Point out each leukocyte.
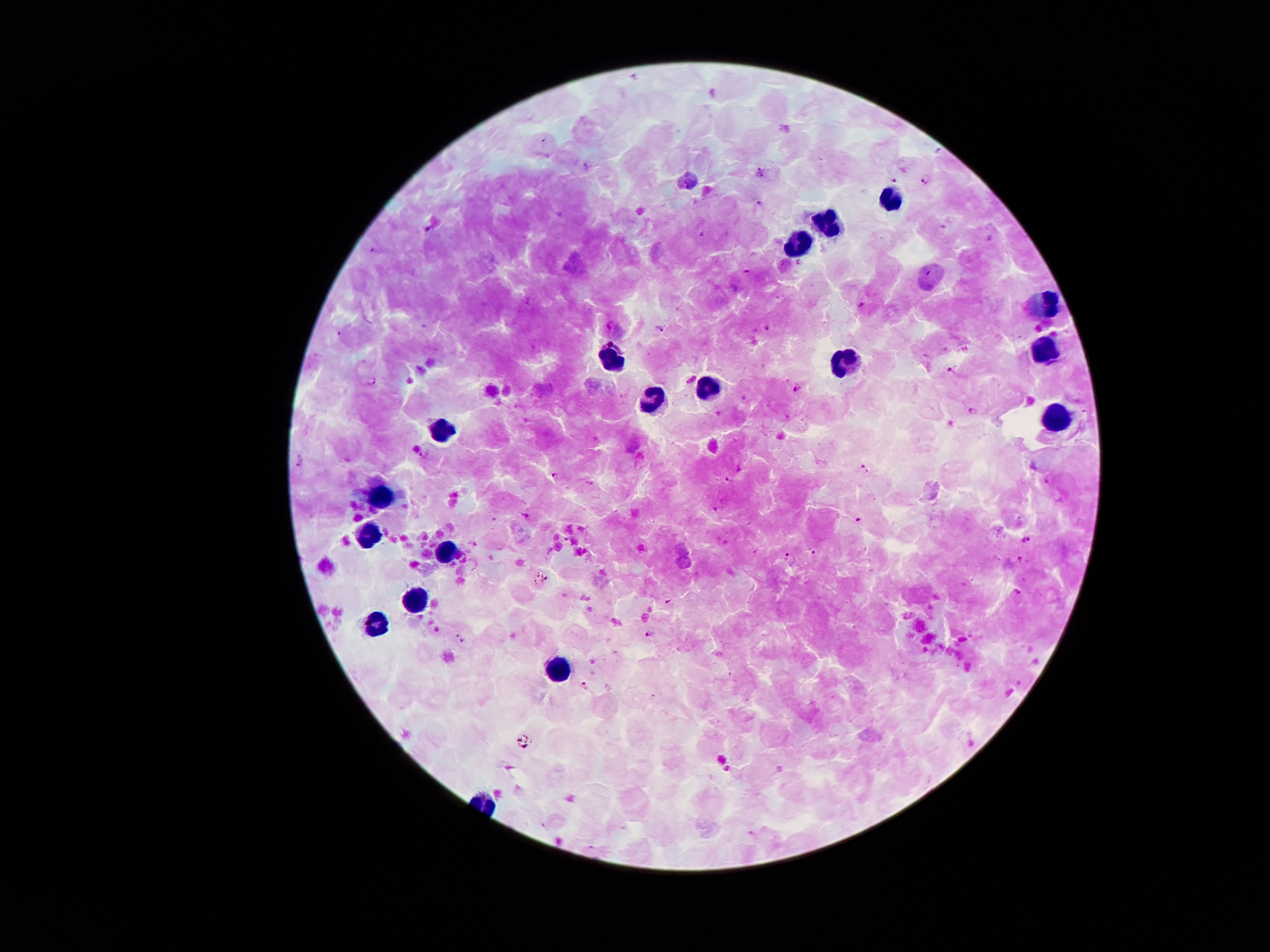

Approximate object centers, in pixels from the top-left corner.
Leukocytes: (x=890, y=198), (x=831, y=224), (x=798, y=244), (x=1047, y=302), (x=1045, y=349), (x=613, y=357), (x=849, y=360), (x=710, y=390), (x=652, y=402), (x=1057, y=417), (x=440, y=430), (x=385, y=494), (x=369, y=538), (x=450, y=555), (x=416, y=601), (x=375, y=627), (x=554, y=668).

{
  "field_of_view": "single",
  "capture": "smartphone through the microscope eyepiece",
  "patient_malaria_status": "positive for Plasmodium falciparum",
  "malaria_parasite_locations": "approximate object centers, in pixels from the top-left corner: (x=587, y=167), (x=763, y=167), (x=759, y=175), (x=928, y=179), (x=894, y=180), (x=759, y=203), (x=429, y=229), (x=704, y=235), (x=747, y=271), (x=863, y=305), (x=661, y=328), (x=768, y=328), (x=340, y=335), (x=953, y=370), (x=372, y=382), (x=797, y=389), (x=745, y=397), (x=973, y=412), (x=424, y=457), (x=301, y=462), (x=866, y=468), (x=555, y=475), (x=728, y=480), (x=715, y=509), (x=857, y=520), (x=1026, y=539), (x=756, y=552), (x=814, y=553), (x=790, y=558), (x=1019, y=558), (x=1018, y=591), (x=670, y=600), (x=648, y=633), (x=586, y=685)",
  "magnification": "100x",
  "image_size": "1270×952 pixels",
  "preparation": "thick blood smear",
  "stain": "Giemsa"
}